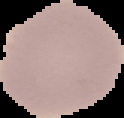
preparation = thin blood film
image size = 124×118 pixels
malaria status = uninfected
image type = segmented cell region with the area outside set to black